Assess this cell for malaria.
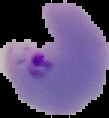
Parasitized.

Summary:
  - Image type: segmented cell region with the area outside set to black
  - Preparation: thin blood smear
  - Image size: 109×118 pixels